Locate every Plasmodium parasite.
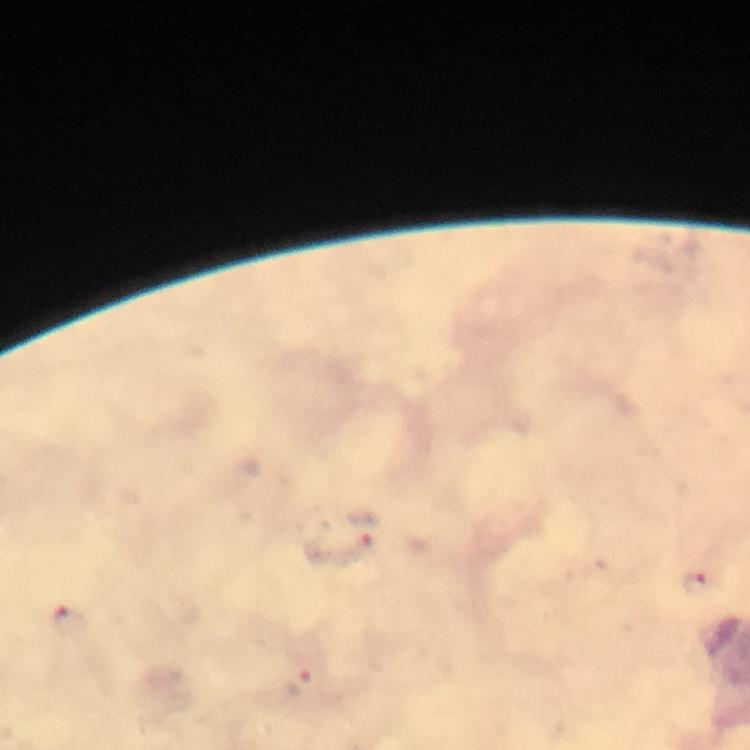
Approximate object centers, in pixels from the top-left corner.
Plasmodium parasites: (x=365, y=529), (x=699, y=584), (x=68, y=621), (x=298, y=682).

Summary:
  - Cropped from: one field of view
  - Stain: Giemsa
  - Immersion oil: applied
  - Context: from a malaria diagnostic workup
  - Preparation: thick smear
  - Image size: 750×750 pixels
  - Capture: smartphone mounted on the microscope
  - Magnification: 100x